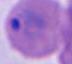
Summary:
  - Identification: Plasmodium
  - Modality: photomicrograph
  - Magnification: 400x or 1000x